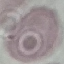

result = negative for malaria parasites
stain = Giemsa
image type = automatically extracted cell patch, resized to 64 × 64 pixels
preparation = thin blood film
capture = smartphone through the microscope eyepiece